Assess this cell for malaria.
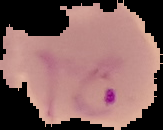
It is parasitized.

Segmented cell region on a black background. From a thin blood smear. Image is 163×130 pixels.